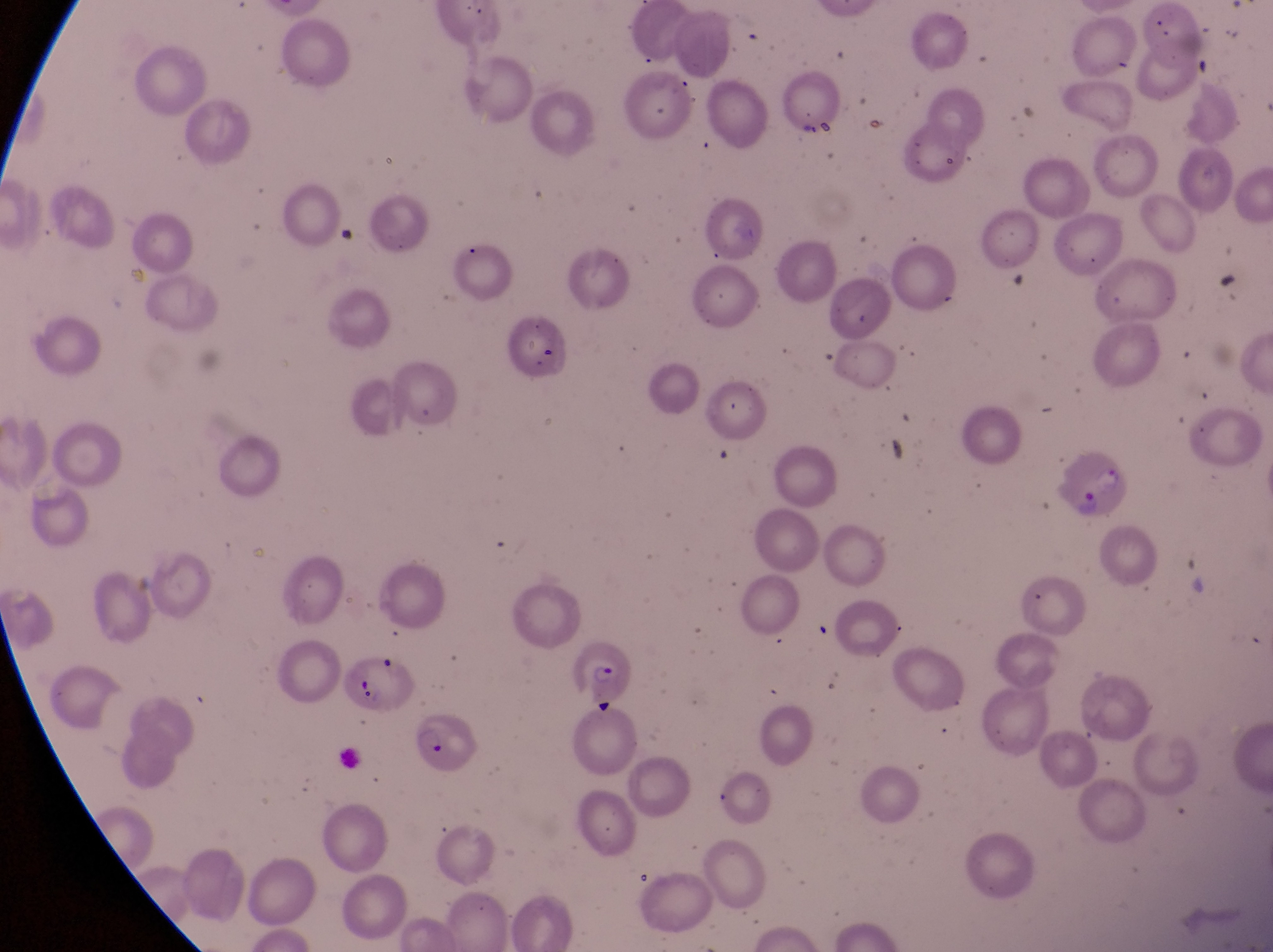

Approximate bounding boxes as (left, top, right, bottom) in pixels.
Summary:
  - Parasitised red blood cell locations: (1061, 437, 1130, 519), (572, 637, 634, 702), (410, 712, 485, 770)
  - Artifact (platelet-like body, stain precipitate, or debris) locations: (356, 675, 389, 714)
  - Magnification: 1000x
  - Field of view: single
  - Preparation: thin blood smear
  - Country: Uganda
  - Capture: smartphone photograph through the eyepiece of an Olympus CX-23 microscope
  - Image size: 1273×952 pixels